Name the parasite shown.
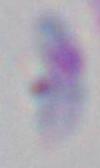
Toxoplasma gondii.

Captured at 1000x magnification. Photomicrograph.